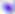

400x magnification. Toxoplasma gondii is seen. Micrograph.